Name the cell type shown.
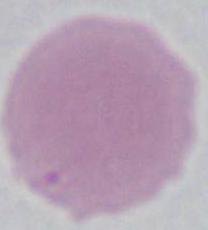

An erythrocyte.

Photomicrograph. 1000x magnification.